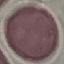
Result: no malaria parasites detected. Giemsa stain. Acquired by smartphone through the microscope eyepiece. Thin blood film. Cell patch, automatically extracted from a larger field of view and resized to 64 × 64 pixels.